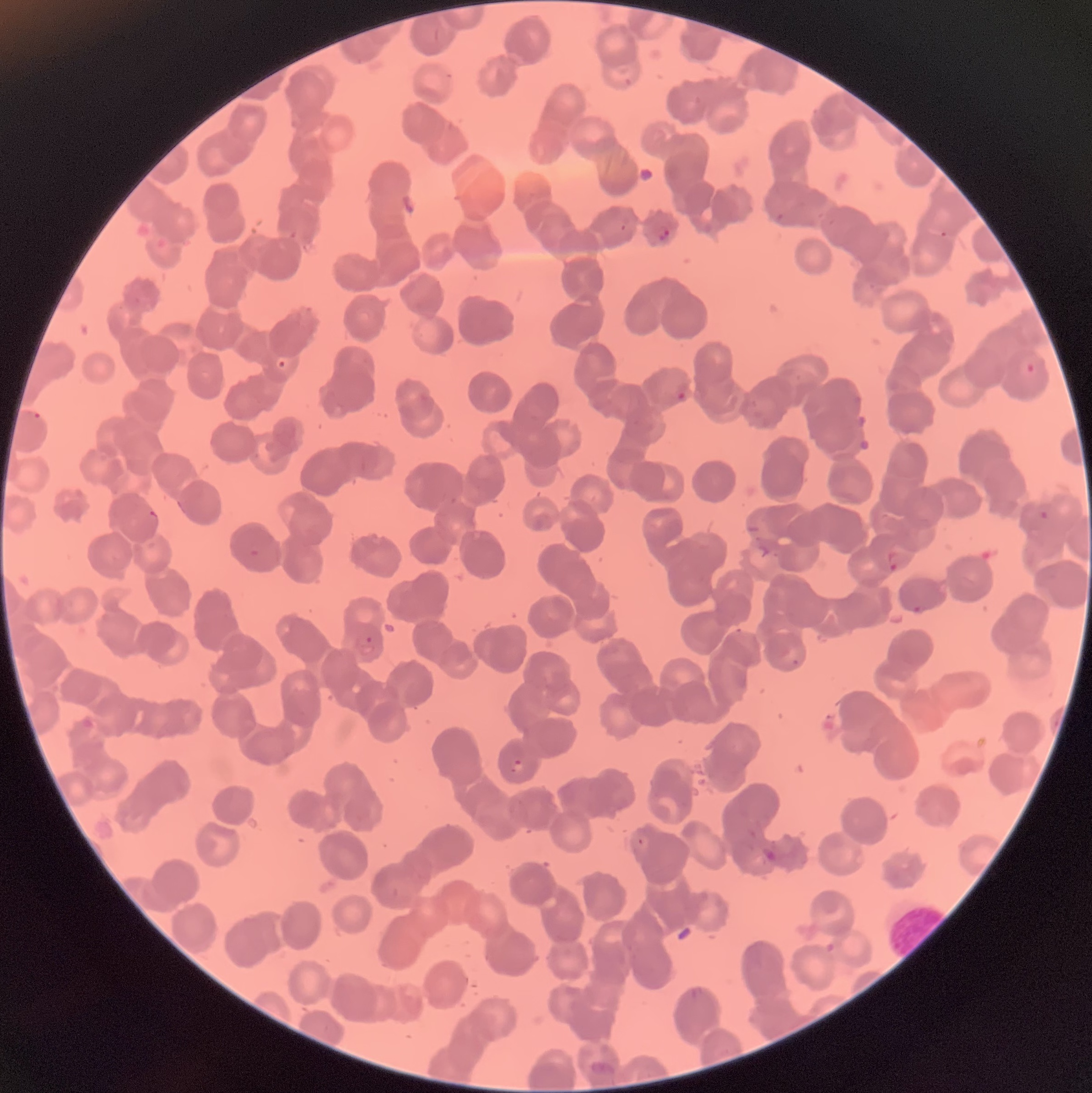

Approximate bounding boxes as [x1, y1, x2, y2] in pixels. Plasmodium parasites too small for a box (approximate centers as [x, y] in pixels): [943, 234]. Plasmodium parasite locations: [775, 212, 783, 222], [620, 223, 627, 231], [655, 226, 671, 240], [275, 358, 290, 370], [1021, 359, 1037, 376], [675, 391, 687, 401], [32, 412, 43, 422], [148, 510, 158, 524], [1039, 510, 1048, 520], [250, 549, 259, 558], [887, 550, 907, 572], [912, 605, 926, 614], [735, 628, 755, 650], [365, 636, 374, 645], [785, 650, 801, 665], [508, 759, 529, 778], [637, 837, 652, 850], [762, 847, 777, 861], [686, 988, 706, 1000]. The red blood cells show rouleaux formation. Thin blood film. Optical microscopy. Image is 1092×1093 pixels.